Give the extent of all Plasmodium malariae-infected red blood cells.
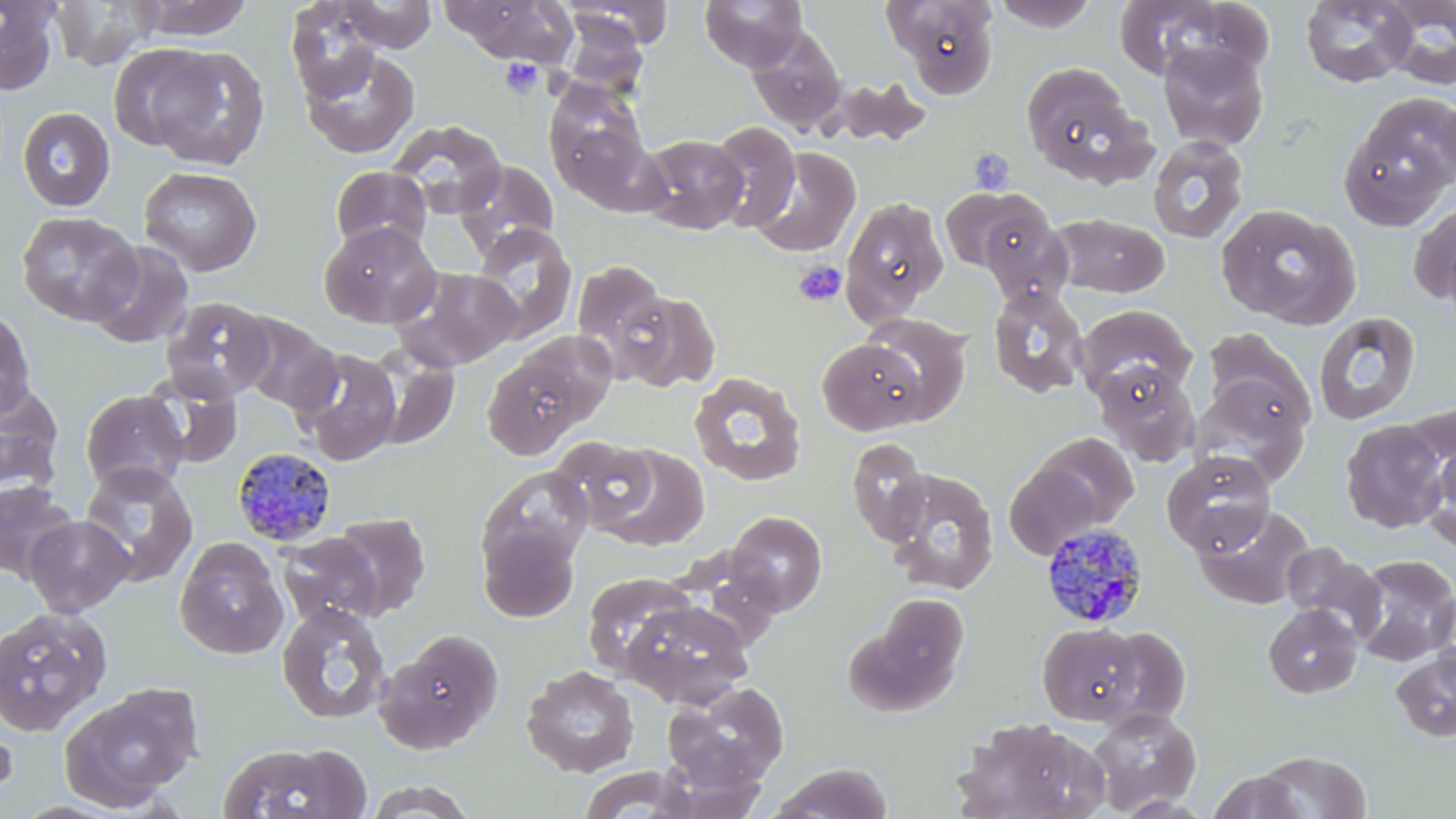
Approximate bounding boxes as (x1,y1)-(x2,y2) corner pairs in pixels.
Plasmodium malariae-infected red blood cells: (232,448)-(338,546), (1038,524)-(1146,631).

Summary:
  - Uninfected red blood cell locations: (0,0)-(60,94), (48,0)-(164,71), (133,0)-(254,40), (337,0)-(437,52), (699,0)-(809,71), (885,0)-(1001,98), (1109,0)-(1243,82), (286,1)-(388,100), (441,1)-(574,65), (564,1)-(673,49), (991,1)-(1101,32), (1301,1)-(1416,88), (1381,1)-(1456,90), (559,12)-(649,97), (746,25)-(847,134), (107,42)-(216,152), (1158,42)-(1269,151), (299,46)-(420,159), (146,47)-(270,172), (1020,65)-(1149,184), (819,76)-(931,149), (543,81)-(654,201), (1435,93)-(1456,191), (1340,96)-(1456,228), (17,106)-(116,212), (387,118)-(507,219), (707,120)-(801,232), (638,134)-(749,234), (1147,135)-(1249,243), (750,147)-(861,257), (455,160)-(559,259), (330,165)-(432,255), (138,166)-(262,276), (940,186)-(1048,273), (840,197)-(950,322), (1409,199)-(1456,307), (1215,203)-(1360,328), (16,211)-(142,327), (980,211)-(1074,308), (1050,212)-(1170,297), (319,222)-(441,328), (469,223)-(578,344), (87,241)-(194,349), (571,259)-(670,373), (392,266)-(521,371), (988,285)-(1089,399), (616,289)-(721,393), (161,297)-(275,402), (1073,304)-(1196,402), (0,309)-(37,421), (1314,311)-(1421,425), (233,312)-(342,415), (861,313)-(972,424), (1204,329)-(1313,431), (816,338)-(928,436), (294,345)-(402,465), (366,346)-(460,451), (482,349)-(594,459), (1094,362)-(1200,467), (139,370)-(243,469), (689,371)-(807,486), (1190,380)-(1309,483), (0,381)-(64,498), (80,389)-(189,495), (1403,406)-(1456,519), (1340,419)-(1451,532), (1033,433)-(1140,529), (549,435)-(660,533), (846,437)-(930,546), (587,442)-(711,551), (1423,443)-(1456,555), (1161,450)-(1275,555), (1005,461)-(1106,558), (79,462)-(198,586), (478,466)-(594,579), (882,468)-(1000,596), (0,480)-(78,582), (1191,503)-(1314,610), (725,510)-(828,615), (329,512)-(432,619), (24,515)-(134,617), (477,522)-(582,622), (275,533)-(383,630), (174,537)-(289,660), (1281,541)-(1386,641), (1351,554)-(1456,666), (581,571)-(698,680), (874,593)-(970,693), (622,599)-(754,708), (275,602)-(392,725), (1263,603)-(1363,699), (0,605)-(113,737), (1037,622)-(1142,725), (1099,626)-(1191,727), (377,628)-(504,753), (1391,646)-(1456,742), (520,664)-(640,777), (662,680)-(789,791), (60,682)-(202,811), (1086,707)-(1201,814), (0,713)-(18,810), (953,717)-(1105,819), (217,741)-(372,819), (1255,750)-(1371,818), (768,762)-(894,819), (573,766)-(703,819), (1208,770)-(1307,818), (361,779)-(480,819)
  - Platelet locations: (500,57)-(543,98), (968,148)-(1016,196), (794,261)-(846,306)
  - Slide-level diagnosis: Plasmodium malariae
  - Stain: May-Grünwald-Giemsa
  - Preparation: thin blood smear
  - Field of view: one of a larger specimen
  - Modality: light microscopy
  - Image size: 1456×819 pixels
  - Magnification: 1000x